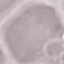
malaria status = uninfected
preparation = thin smear
image type = automatically extracted cell patch, resized to 64 × 64 pixels
stain = Giemsa
capture = smartphone through the microscope eyepiece